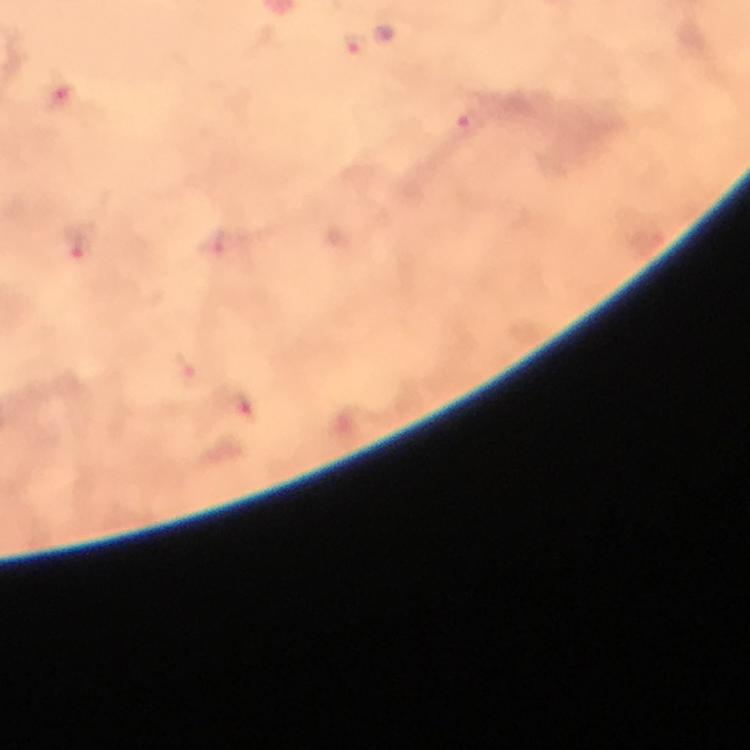

Approximate centers as [x, y] in pixels.
Summary:
  - Plasmodium parasite locations: [355, 43], [65, 101], [471, 123], [76, 244], [212, 244], [182, 368], [245, 407]
  - Magnification: 100x
  - Preparation: thick blood smear
  - Stain: Giemsa
  - Cropped from: a single field of view
  - Context: from a diagnostic examination for malaria
  - Immersion oil: used
  - Capture: smartphone mounted on the microscope
  - Image size: 750×750 pixels